Assess this cell for malaria.
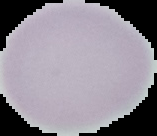
It is uninfected.

{
  "preparation": "thin blood smear",
  "image_size": "157×136 pixels",
  "image_type": "segmented cell region with the area outside set to black"
}